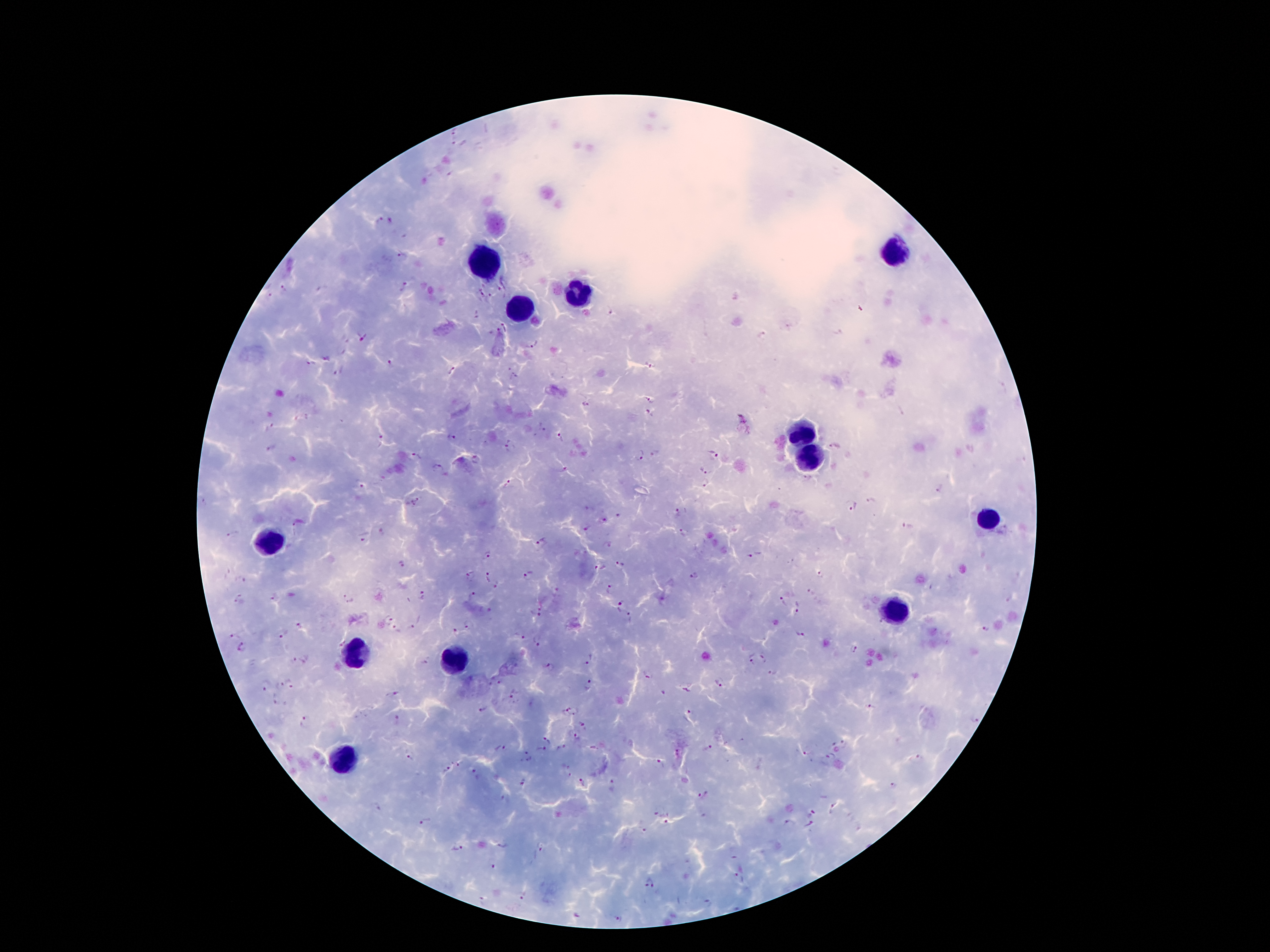 Approximate centers as [x, y] in pixels. Leukocyte locations: [894, 248], [487, 262], [577, 296], [520, 307], [800, 433], [808, 460], [989, 519], [268, 544], [894, 611], [356, 653], [453, 664], [342, 760]. Malaria parasite locations: [454, 131], [455, 143], [449, 175], [379, 219], [401, 255], [284, 287], [404, 287], [501, 288], [267, 292], [478, 293], [491, 296], [613, 311], [476, 313], [506, 326], [498, 332], [761, 336], [362, 338], [531, 344], [310, 363], [390, 363], [651, 365], [339, 370], [453, 371], [513, 375], [651, 397], [586, 405], [650, 413], [452, 436], [561, 439], [380, 441], [510, 447], [834, 447], [655, 452], [713, 454], [639, 455], [414, 456], [477, 460], [439, 467], [564, 468], [704, 471], [707, 484], [508, 485], [360, 487], [939, 488], [871, 500], [415, 501], [851, 506], [677, 513], [618, 516], [603, 520], [299, 524], [907, 526], [587, 529], [231, 533], [683, 533], [363, 534], [541, 541], [609, 545], [487, 555], [750, 556], [622, 563], [403, 565], [603, 567], [694, 574], [819, 574], [470, 575], [528, 576], [488, 577], [497, 586], [607, 587], [554, 592], [273, 596], [423, 596], [469, 597], [347, 598], [238, 599], [782, 603], [620, 604], [799, 608], [536, 614], [629, 616], [388, 618], [300, 624], [469, 624], [414, 626], [984, 628], [396, 629], [456, 631], [230, 634], [283, 635], [802, 635], [520, 637], [538, 640], [244, 648], [855, 648], [766, 658], [590, 660], [299, 661], [749, 663], [551, 669], [774, 672], [647, 675], [720, 681], [278, 684], [292, 684], [589, 684], [266, 685], [663, 691], [395, 693], [515, 693], [276, 699], [870, 707], [481, 710], [570, 710], [690, 711], [395, 718], [305, 721], [582, 722], [576, 736], [546, 739], [845, 743], [834, 745], [499, 747], [540, 749], [562, 749], [708, 749], [679, 753], [809, 754], [528, 757], [408, 758], [832, 758], [919, 760], [458, 763], [659, 763], [448, 770], [474, 770], [566, 774], [522, 782], [582, 782], [614, 785], [893, 786], [704, 795], [376, 808], [832, 808], [654, 813], [811, 813], [425, 822], [666, 822], [790, 824], [809, 826], [644, 831], [503, 844], [457, 848], [540, 848], [493, 868], [740, 878], [649, 883], [520, 895], [483, 901], [618, 917]. Image is 1270×952 pixels. Patient malaria status: positive for Plasmodium falciparum. One field from this slide. 100x magnification. Smartphone photograph taken through the microscope eyepiece. Giemsa stain. Thick peripheral-blood smear.